State which parasite is depicted.
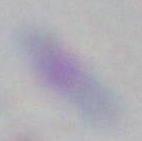

This is Toxoplasma gondii.

Micrograph. 1000x magnification.